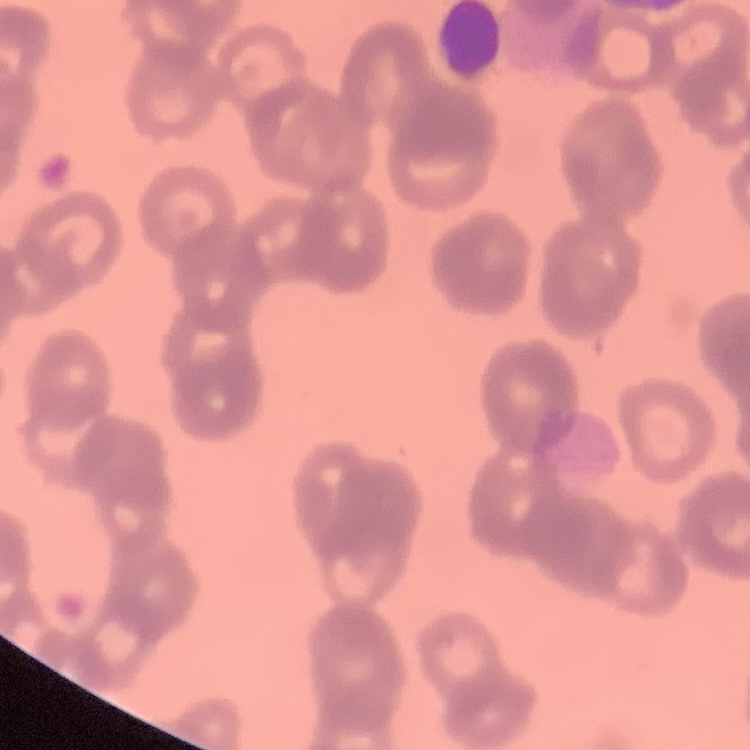
The red blood cells show rouleaux formation. Square crop of a larger photomicrograph. Field's or Giemsa stain. Thin blood film.